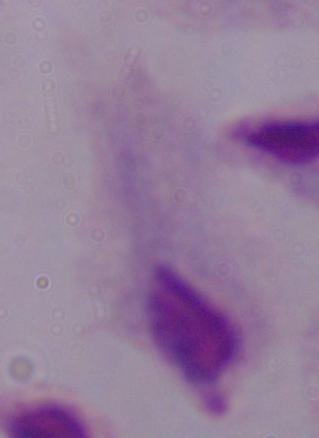
Summary:
  - Identification: trichomonad
  - Modality: micrograph
  - Magnification: 1000x